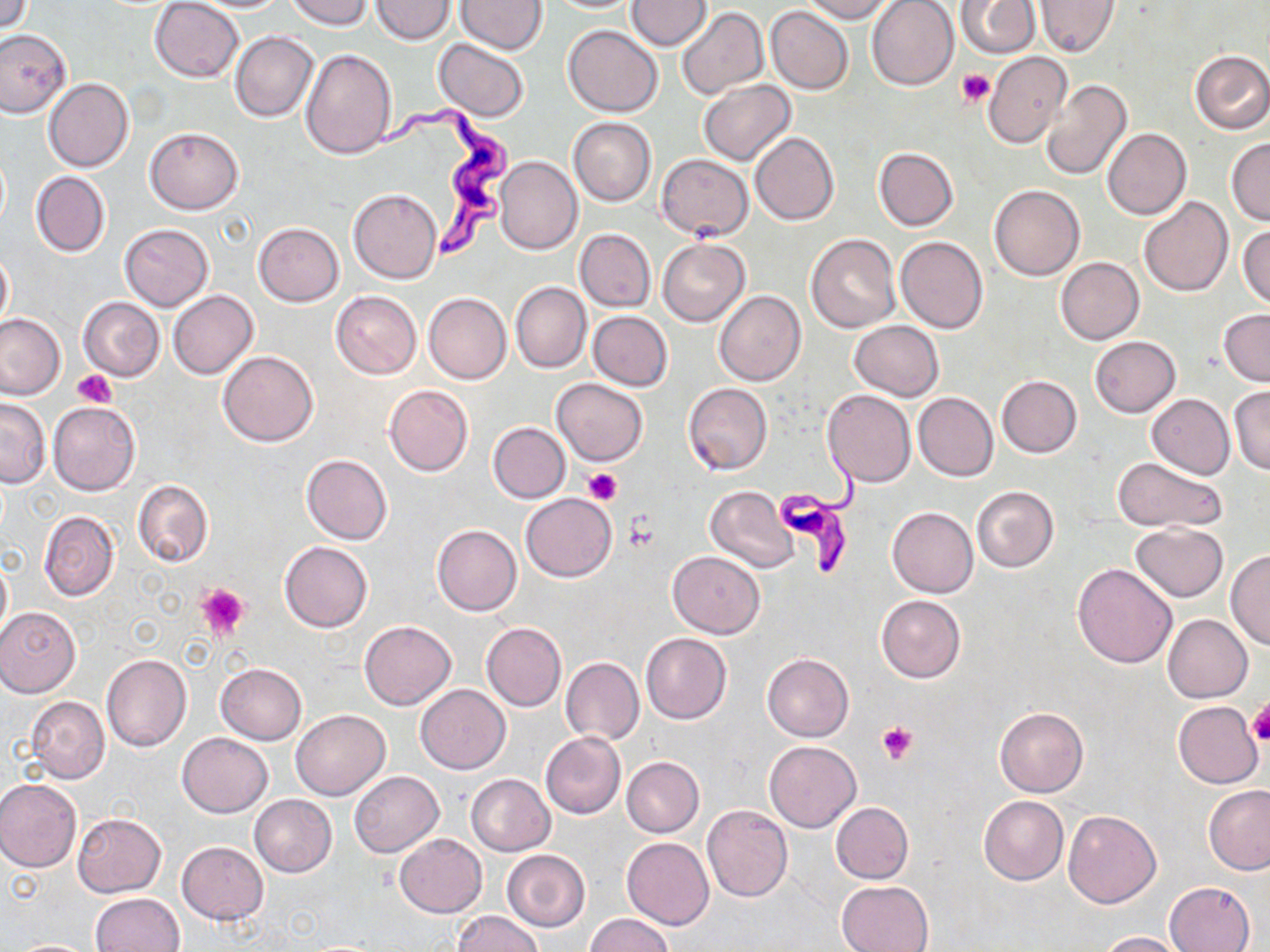
slide-level diagnosis = Trypanosoma brucei
magnification = 1000x
field of view = one of a larger specimen
uninfected red blood cell locations = approximate bounding boxes as (x1,y1)-(x2,y2) corner pairs in pixels: (150,0)-(244,82), (286,0)-(373,30), (370,0)-(456,43), (626,0)-(712,50), (800,0)-(894,22), (867,0)-(958,90), (957,0)-(1039,59), (1035,0)-(1118,58), (0,1)-(32,35), (456,1)-(548,55), (767,5)-(853,95), (677,6)-(768,98), (563,25)-(662,117), (0,28)-(73,118), (230,31)-(319,122), (433,39)-(528,122), (301,47)-(396,158), (1190,50)-(1270,133), (984,51)-(1072,148), (43,78)-(133,172), (1040,79)-(1131,182), (699,80)-(795,165), (568,118)-(656,207), (145,127)-(244,213), (1103,127)-(1191,218), (751,131)-(839,225), (1226,138)-(1270,224), (873,147)-(958,230), (656,153)-(752,240), (495,156)-(582,254), (31,171)-(110,257), (989,185)-(1084,280), (348,188)-(442,283), (1139,197)-(1232,297), (253,223)-(343,306), (1238,223)-(1269,308), (118,224)-(213,311), (576,229)-(655,311), (805,233)-(900,333), (895,236)-(988,335), (658,238)-(749,326), (0,249)-(12,331), (1056,256)-(1144,344), (511,281)-(591,373), (168,290)-(258,379), (714,290)-(806,385), (330,291)-(422,379), (423,293)-(511,384), (78,297)-(164,381), (1219,309)-(1270,384), (589,311)-(673,390), (0,312)-(67,400), (850,320)-(942,400), (1089,336)-(1181,417), (218,351)-(318,447), (996,375)-(1082,458), (551,377)-(647,466), (683,383)-(772,475), (385,384)-(473,476), (1228,386)-(1270,473), (822,389)-(915,487), (1180,390)-(1270,476), (914,392)-(998,481), (1147,394)-(1235,478), (0,398)-(49,488), (48,401)-(140,496), (488,422)-(570,502), (300,454)-(392,545), (292,456)-(381,630), (1113,456)-(1226,532), (133,480)-(213,567), (705,485)-(799,573), (971,486)-(1059,572), (520,493)-(617,581), (887,507)-(978,597), (39,511)-(120,601), (1131,522)-(1228,602), (431,524)-(522,614), (279,541)-(371,633), (1226,548)-(1270,649), (667,551)-(766,639), (0,555)-(11,644), (1071,563)-(1177,668), (876,595)-(966,684), (0,606)-(81,698), (1163,614)-(1253,702), (359,620)-(456,710), (481,622)-(566,711), (640,633)-(732,724), (101,653)-(192,751), (762,653)-(853,741), (561,656)-(643,746), (215,661)-(307,745), (416,685)-(510,774), (25,696)-(110,783), (1174,701)-(1262,787), (994,707)-(1088,796), (290,709)-(389,800), (989,709)-(1076,882), (178,732)-(272,817), (540,732)-(626,819), (764,741)-(861,833), (621,756)-(704,838), (348,771)-(444,857), (466,774)-(556,856), (0,778)-(81,873), (1203,784)-(1270,874), (249,794)-(336,877), (978,795)-(1068,885), (831,802)-(913,883), (702,804)-(793,902), (1063,809)-(1161,908), (72,813)-(165,897), (394,834)-(487,917), (623,837)-(715,930), (177,841)-(269,926), (501,849)-(590,933), (836,880)-(934,951), (1164,882)-(1255,952), (91,892)-(185,952), (451,911)-(545,952), (584,913)-(676,952), (1095,931)-(1186,951), (7,939)-(100,951)
preparation = thin blood film
modality = light microscopy
Trypanosoma brucei locations = approximate bounding boxes as (x1,y1)-(x2,y2) corner pairs in pixels: (368,101)-(521,262), (778,452)-(863,577)
image size = 1270×952 pixels
stain = May-Grünwald-Giemsa
platelet locations = approximate bounding boxes as (x1,y1)-(x2,y2) corner pairs in pixels: (957,69)-(995,106), (72,371)-(115,407), (582,469)-(621,504), (621,514)-(661,552), (196,582)-(249,643), (1246,700)-(1270,746), (876,720)-(920,763)